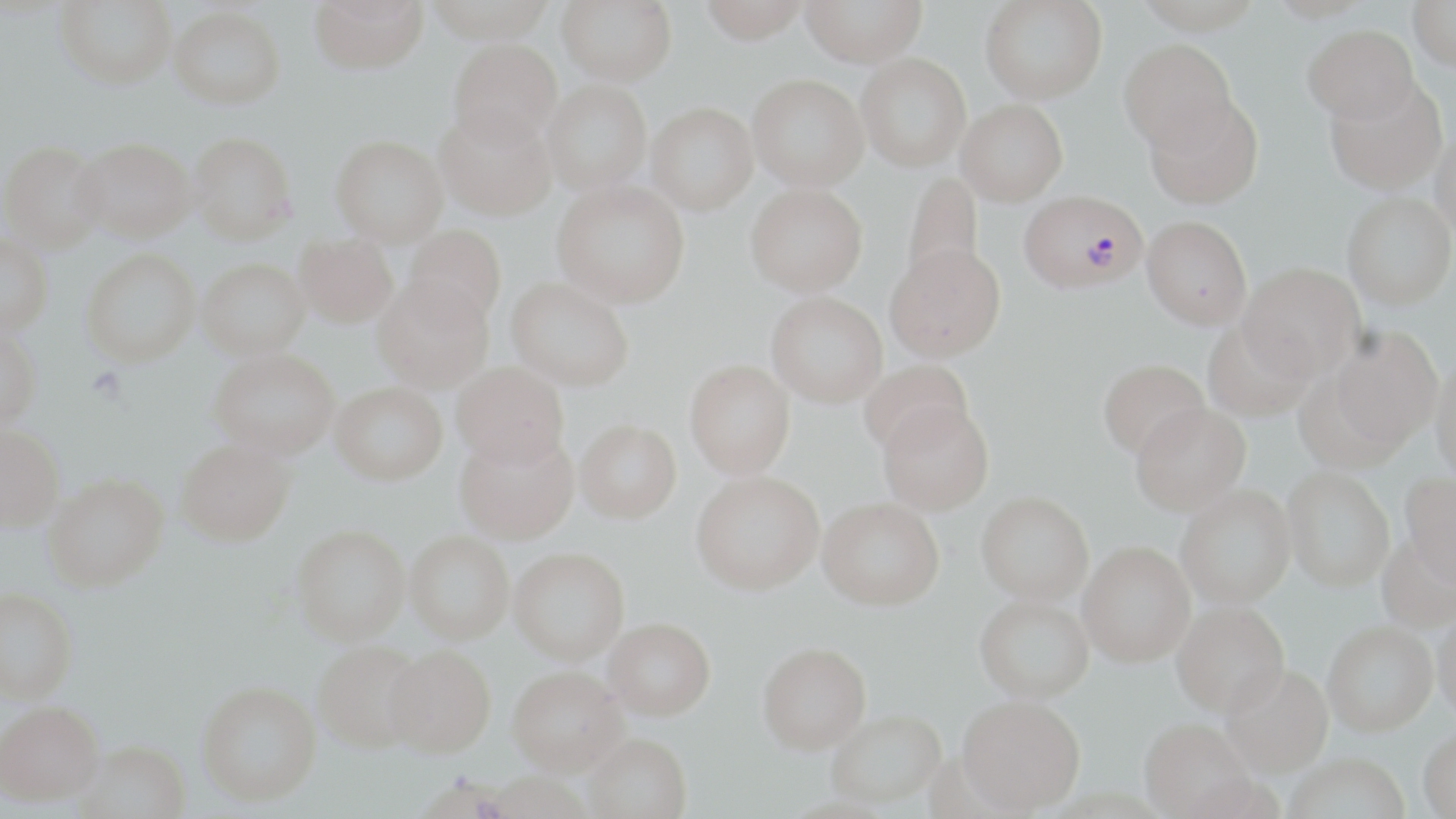

Summary:
  - Coordinate format: approximate bounding boxes as [x1, y1, x2, y2] in pixels
  - Plasmodium falciparum-infected red blood cell locations: [1019, 189, 1147, 292]
  - Uninfected red blood cell locations: [309, 0, 429, 73], [422, 0, 557, 42], [557, 0, 677, 85], [698, 0, 811, 44], [800, 0, 926, 67], [980, 0, 1107, 104], [1409, 0, 1456, 71], [55, 1, 177, 89], [169, 5, 286, 108], [1302, 23, 1420, 123], [449, 38, 562, 151], [1119, 39, 1238, 152], [856, 53, 971, 171], [748, 73, 868, 191], [1323, 77, 1448, 195], [540, 79, 652, 194], [1143, 92, 1263, 209], [957, 100, 1068, 206], [647, 102, 758, 215], [435, 106, 556, 220], [1431, 124, 1456, 243], [189, 132, 298, 244], [331, 135, 448, 245], [73, 137, 195, 242], [2, 140, 107, 253], [901, 171, 985, 289], [552, 179, 690, 307], [745, 182, 868, 296], [1342, 192, 1455, 309], [1141, 215, 1253, 329], [404, 225, 506, 329], [294, 232, 398, 327], [0, 235, 53, 335], [884, 243, 1006, 362], [80, 249, 201, 367], [198, 258, 311, 359], [1239, 262, 1365, 381], [505, 277, 635, 390], [372, 279, 492, 393], [766, 291, 888, 407], [1203, 320, 1315, 421], [1330, 325, 1443, 449], [0, 328, 42, 429], [209, 350, 340, 459], [1430, 356, 1456, 483], [685, 359, 795, 478], [1098, 359, 1209, 459], [860, 360, 973, 458], [452, 361, 569, 468], [331, 382, 446, 485], [878, 399, 994, 514], [1131, 403, 1251, 515], [575, 419, 682, 523], [0, 425, 63, 532], [454, 429, 580, 544], [175, 437, 294, 545], [1283, 466, 1395, 592], [691, 470, 824, 594], [43, 473, 168, 591], [1399, 473, 1456, 588], [1176, 485, 1296, 609], [976, 490, 1093, 604], [818, 497, 944, 609], [291, 524, 410, 643], [406, 530, 514, 643], [1376, 534, 1456, 636], [1077, 542, 1195, 667], [509, 547, 629, 663], [0, 588, 78, 702], [974, 595, 1094, 702], [1172, 603, 1290, 719], [1433, 612, 1456, 729], [603, 617, 716, 720], [1323, 625, 1438, 741], [312, 641, 428, 753], [758, 642, 871, 753], [382, 644, 496, 758], [507, 666, 628, 778], [1221, 667, 1333, 782], [197, 681, 322, 806], [957, 697, 1085, 816], [0, 701, 104, 806], [826, 709, 947, 809], [1140, 722, 1258, 819], [1418, 731, 1456, 819], [583, 734, 691, 819], [76, 740, 190, 819], [1283, 757, 1411, 819]
  - Slide-level diagnosis: Plasmodium falciparum
  - Magnification: 1000x
  - Field of view: single
  - Stain: May-Grünwald-Giemsa
  - Image size: 1456×819 pixels
  - Modality: optical microscopy
  - Preparation: thin blood film